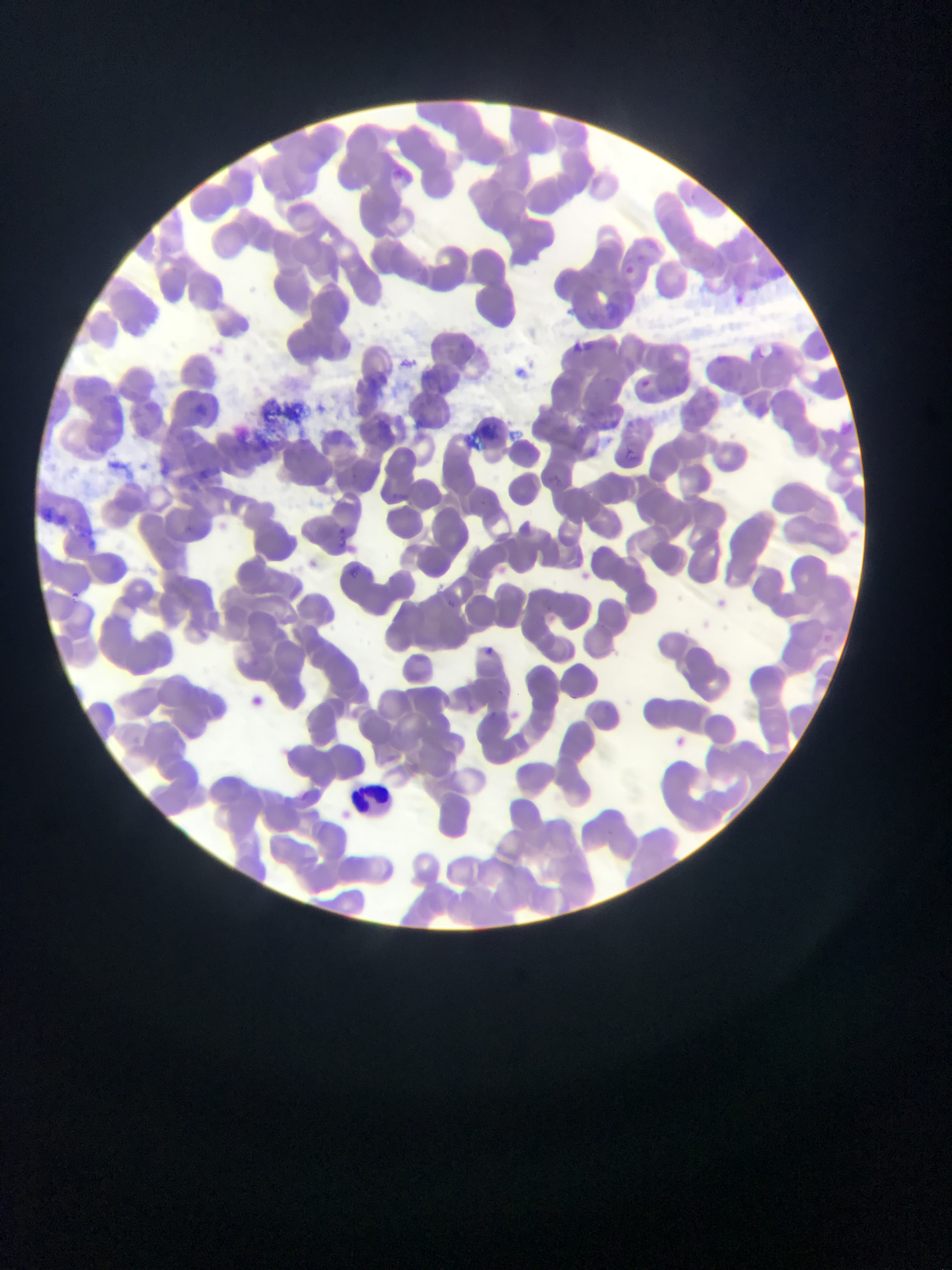 Approximate bounding boxes as (left, top, right, bottom) in pixels. Leukocyte locations: (348, 779, 398, 814). Malaria parasite locations: (617, 261, 639, 281), (726, 290, 750, 313), (631, 373, 656, 396), (626, 447, 638, 459), (350, 566, 361, 580), (70, 588, 78, 602), (449, 595, 462, 609), (483, 643, 496, 655), (239, 686, 276, 717) | approximate (x, y) pixel centers of objects too small to bound: (498, 689). Thin blood film. Mobile-phone photograph taken through the microscope. Collected in Ghana. Image is 952×1270 pixels. Single field of view.